Look for parasitized red blood cells.
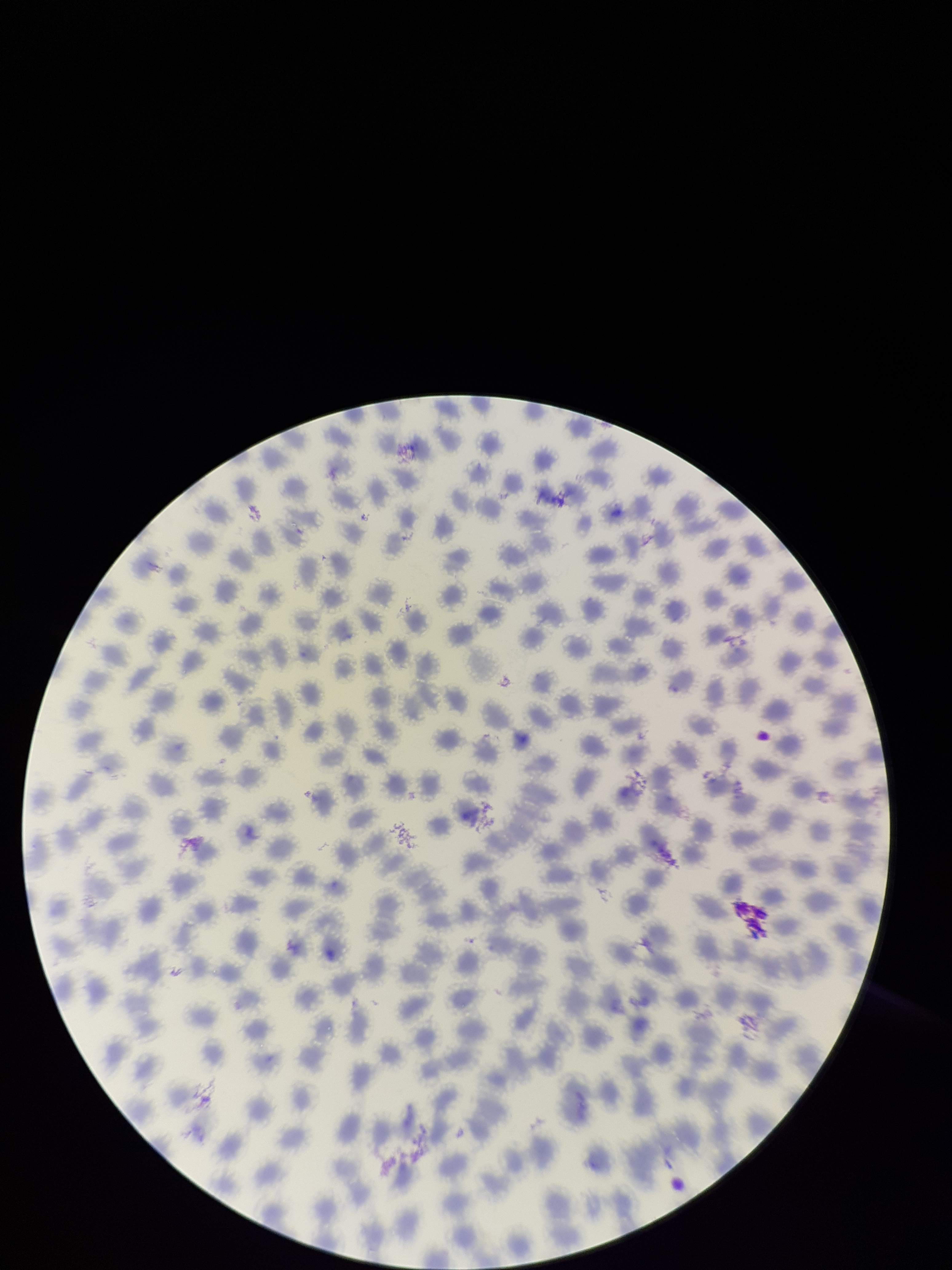

None identified.

{
  "species_reported_for_this_patient": "Plasmodium vivax",
  "field_of_view": "one from this slide",
  "preparation": "thin",
  "stain": "Giemsa",
  "red_blood_cell_count": 281,
  "image_size": "952×1270 pixels",
  "patient_malaria_status": "positive",
  "parasitized_red_blood_cell_count": 0,
  "capture": "smartphone photograph through the microscope eyepiece"
}